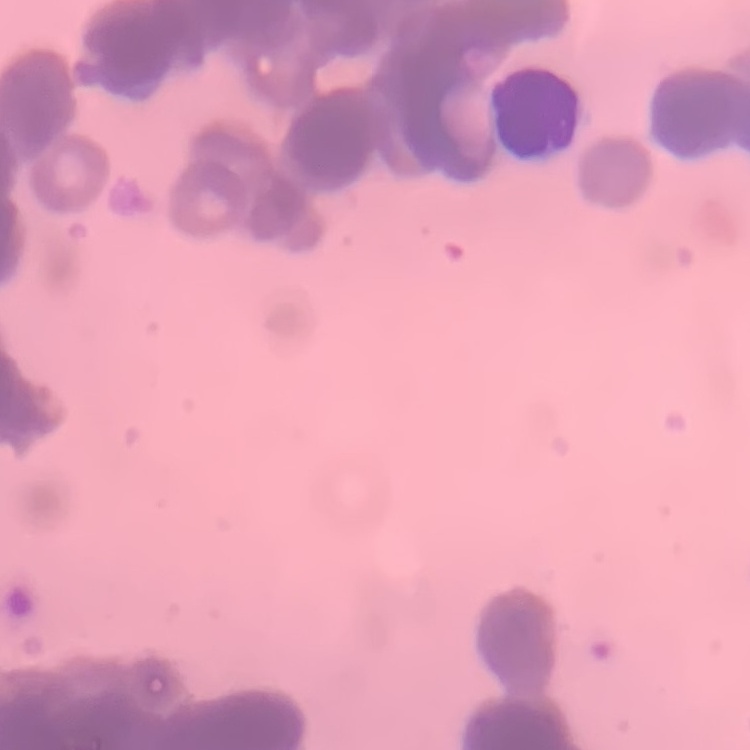 The erythrocytes show rouleaux formation. Thin blood film. One tile cut from a larger photomicrograph. Field's or Giemsa stain.